Assess the morphology of the red blood cells.
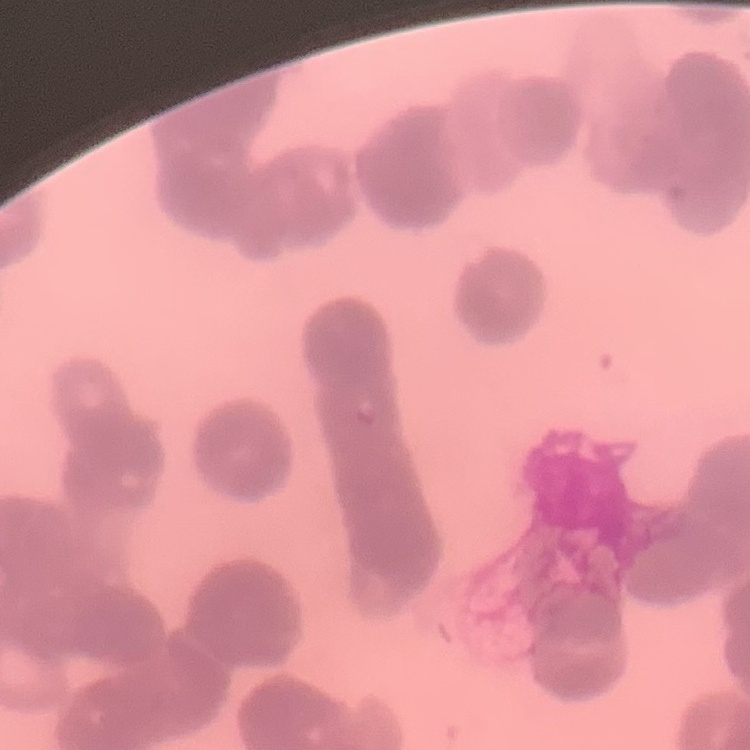

Rouleaux formation.

stain: Field's or Giemsa
preparation: thin peripheral smear
image_type: square crop of a larger photomicrograph